Assess the morphology of the red blood cells.
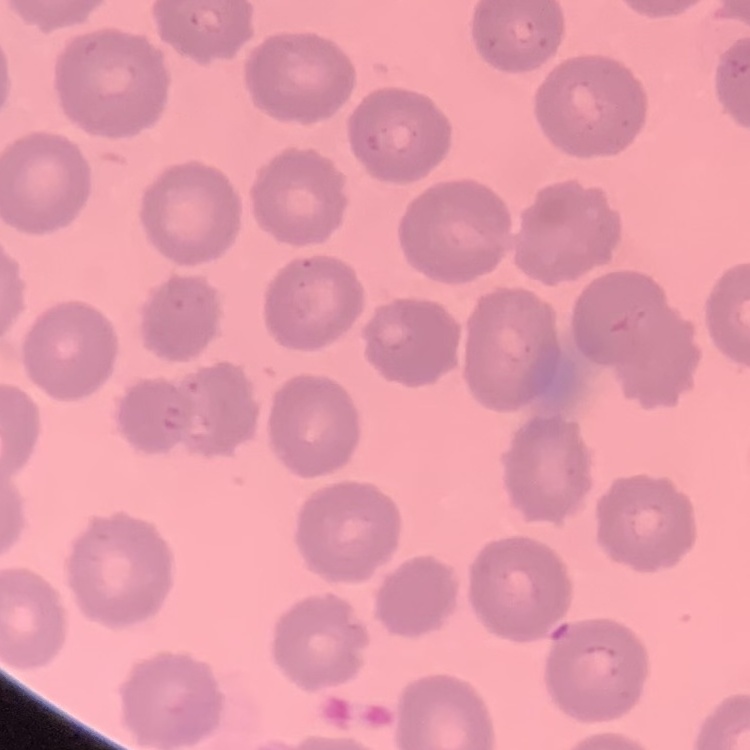

No rouleaux formation.

Summary:
  - Image type: square crop of a larger photomicrograph
  - Stain: Field's or Giemsa
  - Preparation: thin peripheral smear